Classify the preparation.
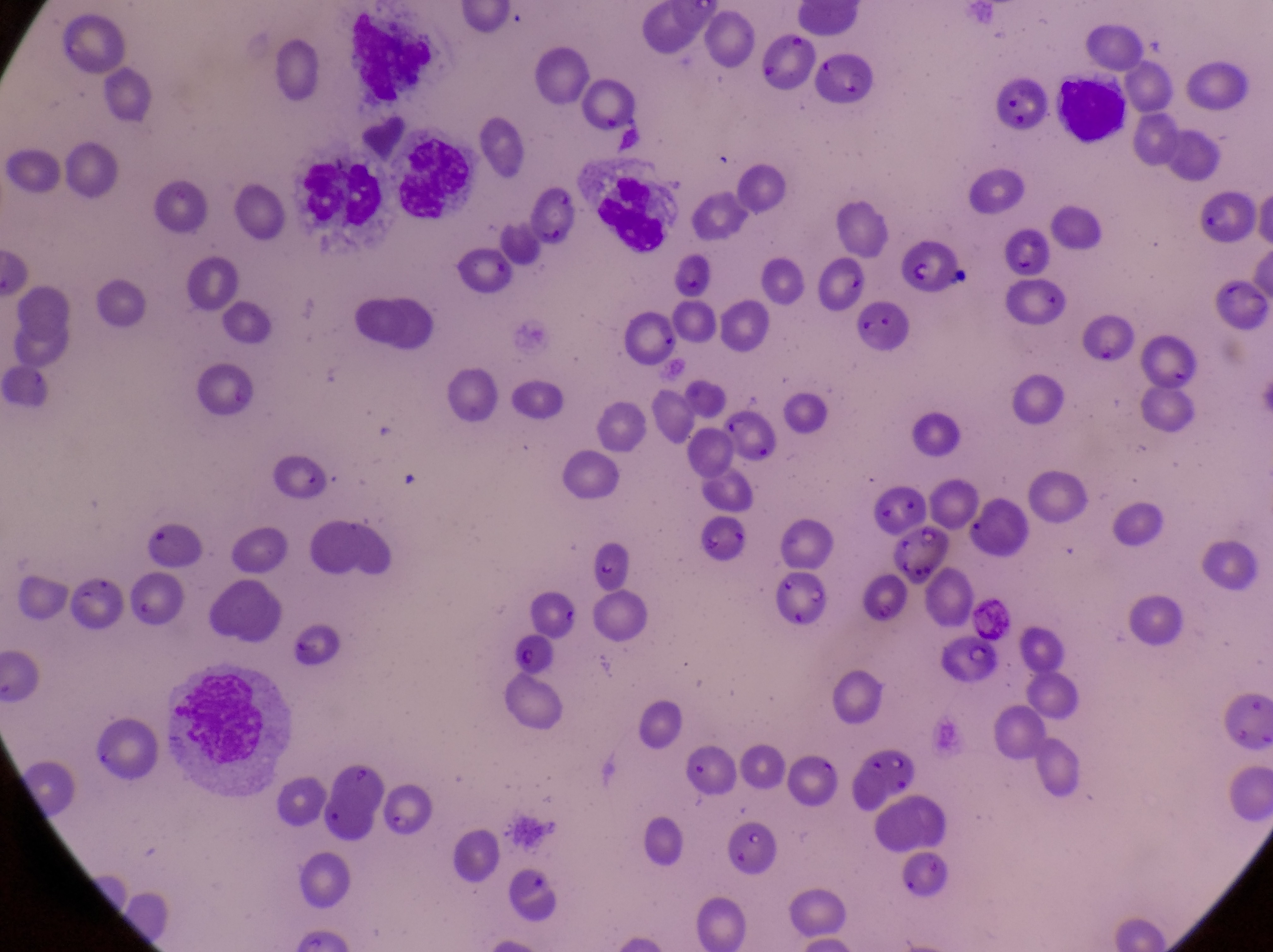

Thin blood smear.

capture = smartphone photograph through the eyepiece of an Olympus CX-23 microscope
country = Uganda
object labeled both leukocyte and artifact (platelet-like body, stain precipitate, or debris) by the source = approximate bounding boxes as [left, top, right, bottom] in pixels: [162, 659, 296, 791]
magnification = 1000x
field of view = single
leukocyte locations = approximate bounding boxes as [left, top, right, bottom] in pixels: [340, 8, 435, 108], [1050, 73, 1129, 148], [392, 127, 484, 237], [302, 160, 389, 237], [588, 165, 673, 268]
parasitised red blood cell locations = approximate bounding boxes as [left, top, right, bottom] in pixels: [809, 47, 876, 112], [904, 239, 951, 299], [854, 295, 911, 357], [128, 569, 190, 627], [761, 569, 824, 632], [938, 640, 996, 688]
image size = 1273×952 pixels